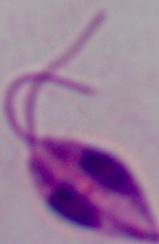
{
  "identification": "Leishmania",
  "magnification": "1000x",
  "modality": "photomicrograph"
}